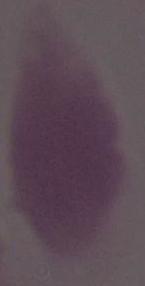

identification = erythrocyte
modality = micrograph
magnification = 1000x